Comment on the morphology of the erythrocytes.
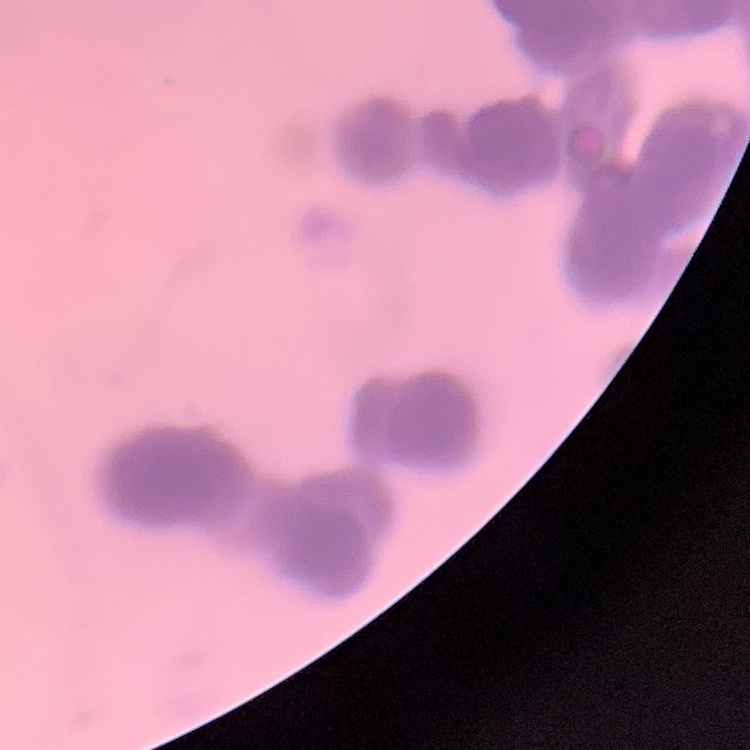
Rouleaux formation.

image type = one tile cut from a larger photomicrograph
stain = Field's or Giemsa
preparation = thin blood smear